Locate every Plasmodium parasite.
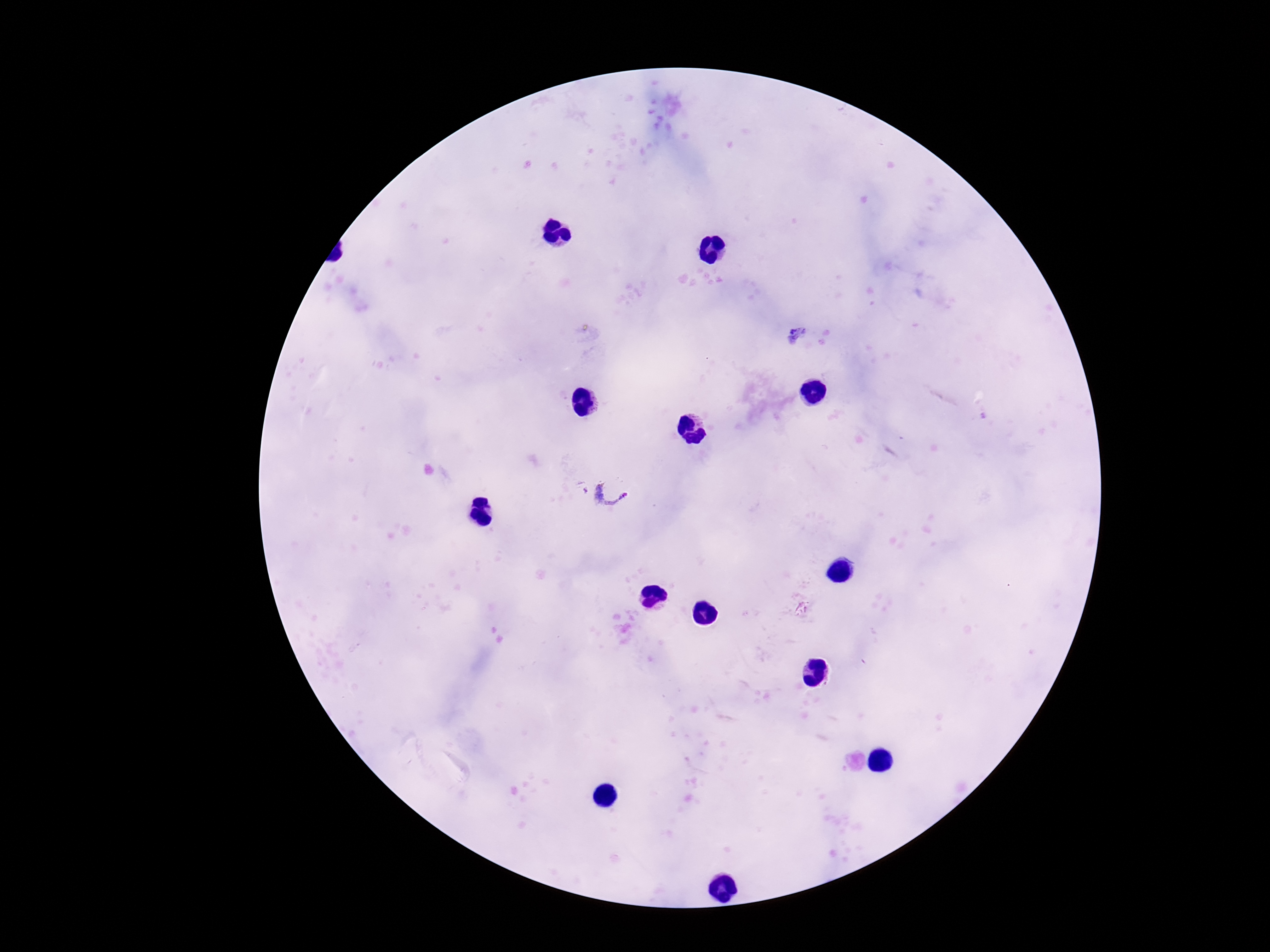
Approximate centers as (x, y) in pixels.
Plasmodium parasites: (798, 336), (609, 492).

image_size: 1270×952 pixels
preparation: thick peripheral-blood smear
patient_malaria_status: positive
stain: Giemsa
magnification: 100x
field_of_view: single
capture: smartphone camera through the microscope eyepiece